Name the blood parasite species.
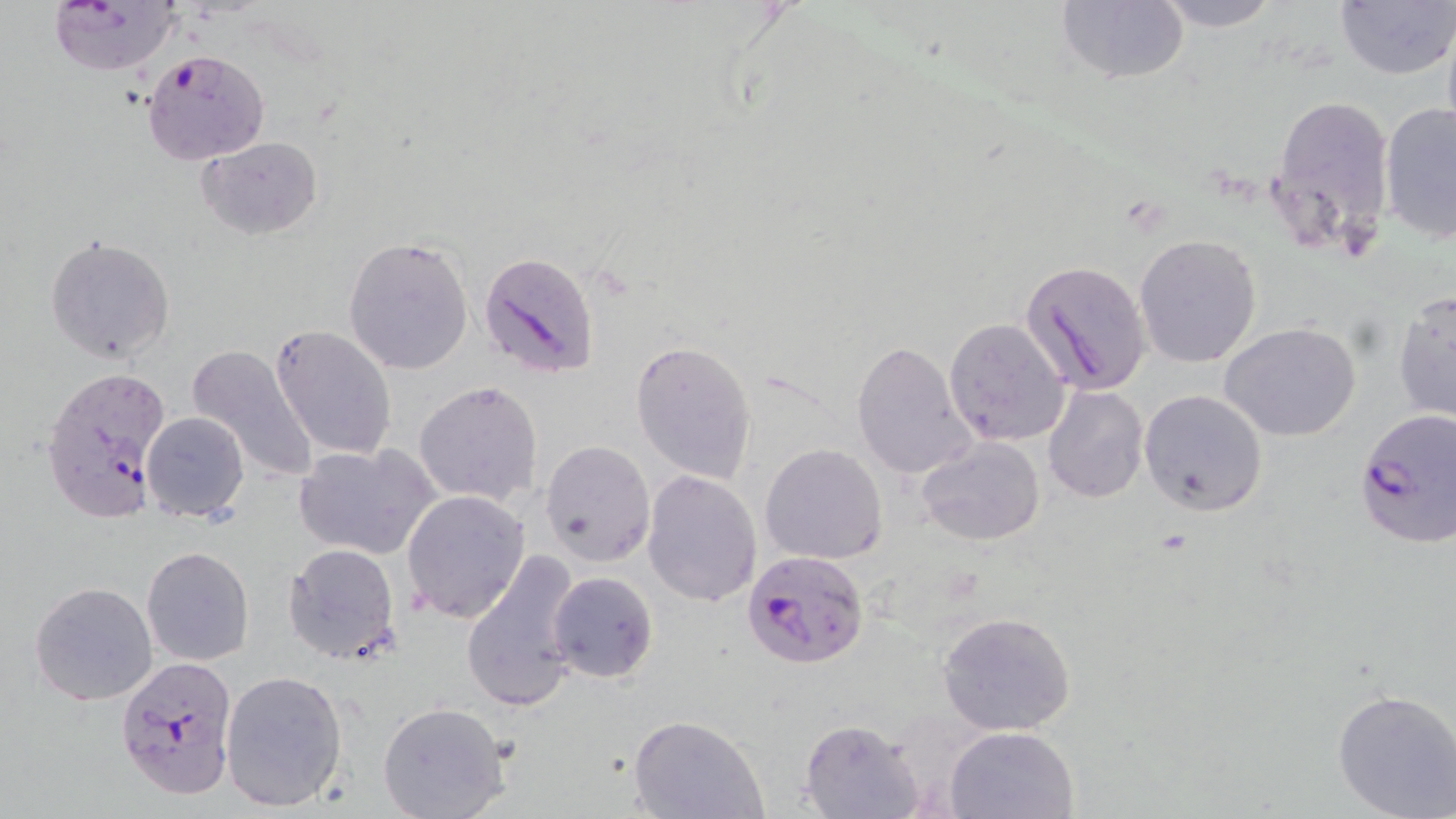

Plasmodium falciparum.

field_of_view: one of a larger specimen
preparation: thin blood smear
image_size: 1456×819 pixels
uninfected_red_blood_cell_locations: 'approximate bounding boxes as (x1, y1, x2, y2) in pixels: (1057, 0, 1188, 85), (1153, 0, 1281, 31), (1333, 1, 1454, 81), (1441, 13, 1456, 148), (1264, 93, 1396, 262), (1378, 101, 1456, 242), (198, 136, 324, 239), (1133, 234, 1261, 369), (46, 235, 175, 364), (343, 235, 475, 375), (1392, 290, 1455, 424), (944, 317, 1072, 447), (1221, 322, 1361, 442), (270, 323, 398, 460), (632, 342, 757, 484), (851, 342, 974, 479), (185, 344, 319, 482), (414, 380, 543, 506), (1043, 385, 1149, 503), (1139, 389, 1269, 516), (140, 411, 250, 522), (916, 438, 1044, 546), (541, 439, 655, 565), (294, 442, 441, 560), (759, 443, 887, 565), (642, 470, 761, 606), (402, 490, 531, 623), (282, 543, 402, 665), (141, 545, 254, 666), (460, 549, 584, 713), (547, 570, 658, 682), (29, 580, 159, 706), (938, 610, 1076, 735), (220, 668, 348, 813), (1331, 686, 1456, 819), (376, 701, 511, 819), (629, 713, 768, 819), (799, 718, 923, 818), (945, 725, 1079, 818)'
plasmodium_falciparum_infected_red_blood_cell_locations: 'approximate bounding boxes as (x1, y1, x2, y2) in pixels: (45, 1, 183, 76), (140, 47, 269, 163), (478, 251, 602, 379), (1018, 260, 1153, 395), (40, 365, 169, 524), (1354, 409, 1456, 550), (743, 549, 870, 667), (114, 654, 237, 801)'
stain: May-Grünwald-Giemsa
magnification: 1000x
modality: optical microscopy